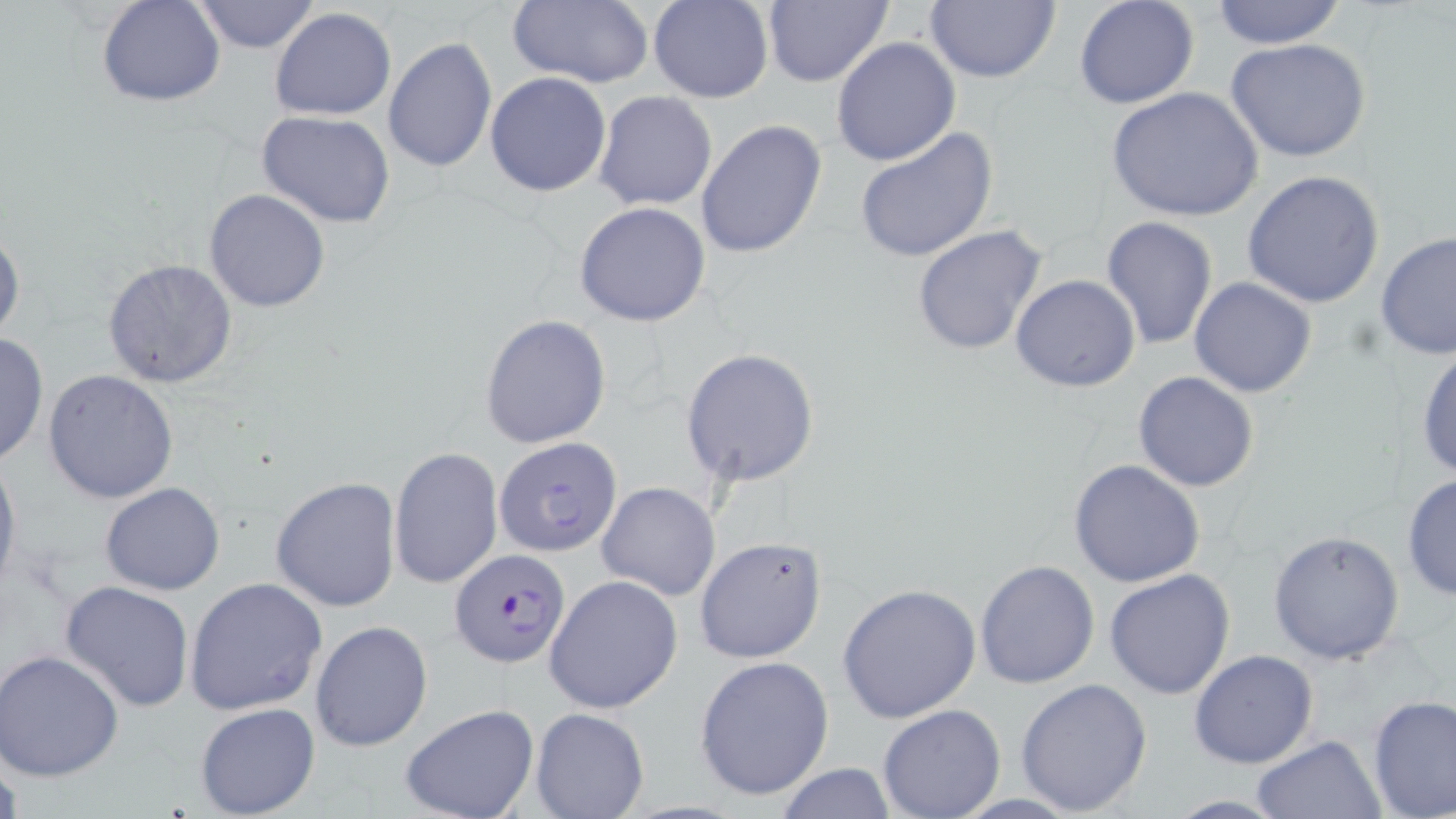
Summary:
  - Coordinate format: approximate bounding boxes as (x1, y1, x2, y2) in pixels
  - Uninfected red blood cell locations: (507, 0, 653, 89), (649, 0, 773, 103), (762, 0, 891, 87), (924, 0, 1061, 83), (1074, 0, 1200, 110), (1210, 0, 1347, 49), (98, 1, 224, 106), (189, 1, 324, 53), (269, 7, 397, 121), (382, 36, 498, 174), (830, 37, 960, 168), (1225, 38, 1371, 162), (485, 72, 612, 197), (1105, 87, 1264, 222), (593, 90, 717, 211), (256, 110, 399, 229), (695, 119, 826, 259), (854, 126, 998, 263), (1241, 169, 1388, 308), (204, 189, 331, 312), (574, 201, 711, 326), (1101, 216, 1218, 352), (0, 224, 24, 346), (911, 225, 1051, 358), (1376, 230, 1455, 360), (101, 259, 238, 388), (1010, 274, 1140, 392), (1189, 276, 1317, 396), (480, 314, 611, 450), (0, 332, 48, 468), (1413, 340, 1456, 482), (680, 347, 821, 488), (44, 369, 180, 504), (1132, 371, 1260, 493), (492, 437, 624, 556), (389, 447, 503, 590), (0, 450, 22, 599), (1067, 459, 1207, 589), (1402, 471, 1456, 602), (270, 477, 402, 611), (101, 482, 225, 596), (598, 482, 720, 601), (1266, 531, 1405, 664), (693, 537, 827, 665), (974, 559, 1101, 688), (1104, 568, 1237, 700), (544, 575, 684, 714), (184, 577, 328, 716), (61, 581, 195, 712), (838, 584, 982, 725), (310, 620, 432, 752), (0, 649, 125, 780), (1189, 649, 1319, 769), (694, 656, 836, 802), (1014, 677, 1152, 817), (1366, 693, 1456, 819), (194, 702, 322, 819), (399, 703, 539, 819), (877, 704, 1006, 818), (530, 707, 650, 819), (1252, 735, 1387, 819), (0, 740, 23, 819), (773, 764, 898, 818), (1159, 795, 1297, 817)
  - Plasmodium falciparum-infected red blood cell locations: (449, 549, 570, 669)
  - Slide-level diagnosis: Plasmodium falciparum
  - Field of view: one of a larger specimen
  - Stain: May-Grünwald-Giemsa
  - Magnification: 1000x
  - Preparation: thin blood film
  - Image size: 1456×819 pixels
  - Modality: light microscopy